Classify this cell by malaria status.
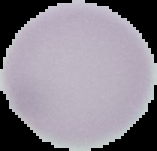
Uninfected.

image size = 157×151 pixels
preparation = thin blood smear
image type = cell region segmented out of the field of view; surrounding area masked to black